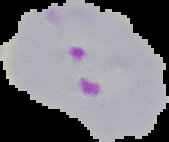
Malaria status: parasitized. Image is 169×142 pixels. Cell region segmented out of the field of view; the surrounding area is masked to black. From a thin blood smear.